Name the cell type shown.
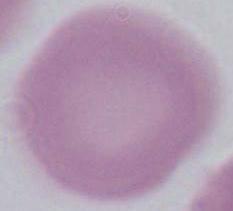

This is an erythrocyte.

modality: photomicrograph
magnification: 1000x